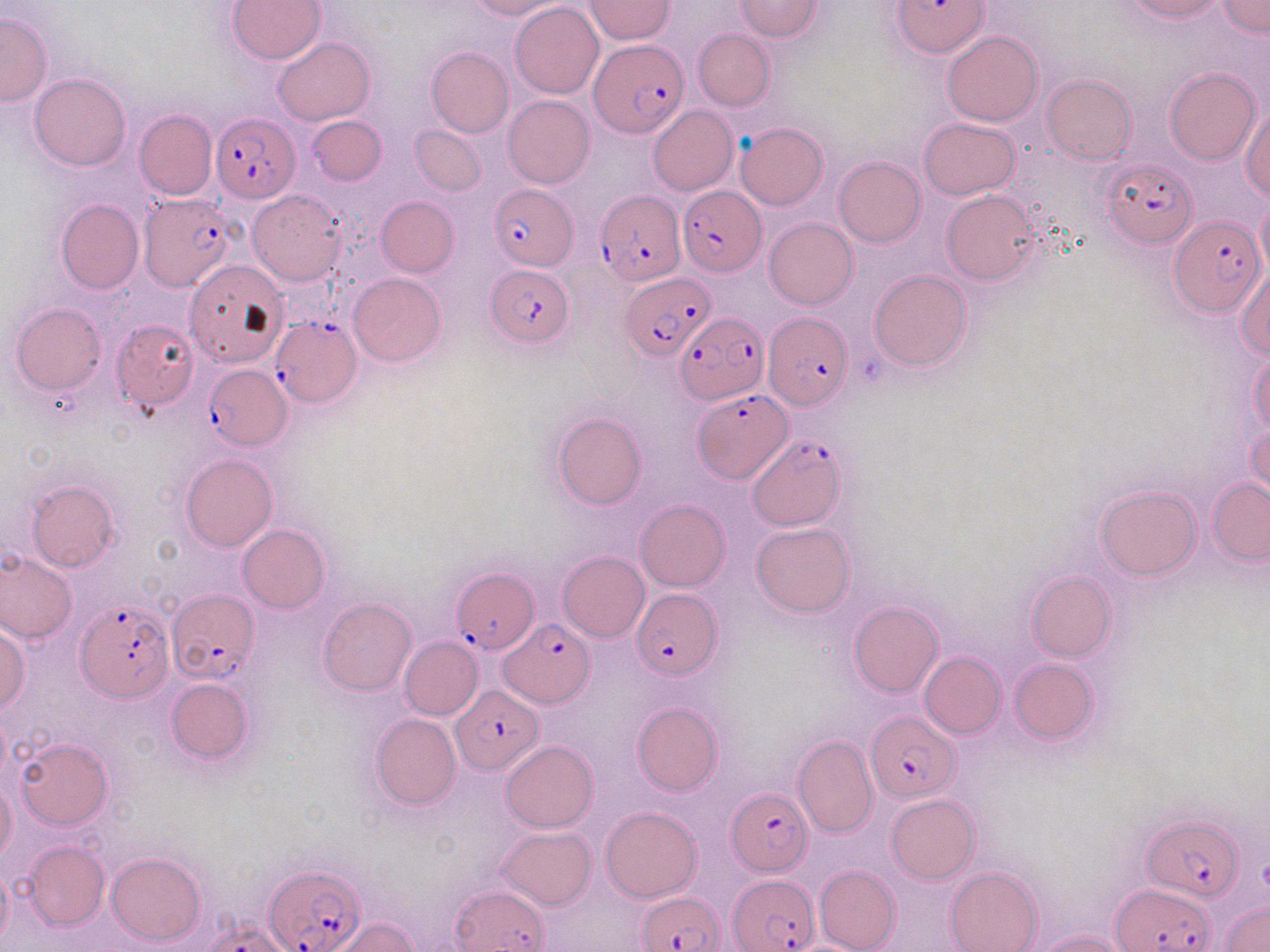
Approximate bounding boxes as (x1, y1, x2, y2) in pixels. Plasmodium falciparum-infected red blood cell locations: (891, 2, 988, 57), (591, 42, 688, 138), (212, 113, 301, 203), (1099, 156, 1198, 249), (489, 185, 579, 271), (677, 186, 763, 276), (597, 190, 685, 286), (140, 195, 234, 290), (1169, 215, 1264, 314), (486, 263, 571, 347), (622, 272, 715, 362), (676, 312, 768, 405), (763, 312, 851, 410), (267, 317, 359, 409), (204, 364, 291, 450), (693, 388, 791, 483), (746, 434, 844, 530), (452, 569, 538, 654), (166, 589, 257, 683), (633, 589, 721, 678), (76, 600, 174, 702), (502, 620, 593, 707), (451, 683, 544, 774), (866, 709, 958, 802), (724, 787, 814, 876), (1145, 814, 1244, 903), (264, 865, 363, 952), (728, 874, 819, 951), (1112, 882, 1214, 952), (639, 893, 724, 952). Uninfected red blood cell locations: (469, 0, 565, 19), (733, 0, 823, 41), (1120, 0, 1226, 22), (1219, 0, 1268, 37), (229, 1, 325, 64), (584, 1, 675, 43), (510, 2, 604, 99), (0, 11, 52, 107), (693, 29, 775, 111), (942, 30, 1042, 126), (273, 37, 374, 125), (426, 47, 513, 138), (1165, 68, 1258, 164), (29, 74, 132, 171), (1042, 74, 1137, 164), (502, 94, 594, 189), (647, 105, 738, 196), (1241, 105, 1270, 200), (135, 109, 218, 201), (307, 116, 386, 186), (919, 117, 1019, 200), (734, 122, 828, 209), (411, 126, 486, 196), (833, 156, 925, 247), (249, 190, 347, 286), (941, 191, 1043, 285), (375, 196, 459, 276), (1256, 196, 1270, 279), (55, 199, 143, 294), (764, 218, 857, 310), (184, 259, 288, 367), (1234, 264, 1270, 359), (868, 269, 971, 371), (348, 273, 445, 366), (12, 302, 106, 394), (111, 320, 198, 411), (1248, 350, 1269, 437), (553, 411, 646, 509), (1246, 418, 1270, 499), (181, 454, 277, 551), (25, 478, 119, 573), (1208, 478, 1270, 564), (1095, 486, 1200, 581), (635, 499, 730, 591), (751, 522, 855, 616), (237, 523, 329, 612), (0, 551, 77, 645), (557, 551, 649, 643), (1026, 571, 1116, 662), (318, 598, 416, 695), (848, 601, 941, 697), (0, 625, 28, 715), (399, 636, 482, 720), (920, 651, 1005, 738), (1009, 658, 1098, 744), (166, 678, 253, 763), (632, 702, 722, 796), (371, 713, 460, 809), (794, 734, 878, 838), (17, 737, 112, 829), (501, 740, 598, 832), (1, 780, 16, 864), (887, 794, 980, 883), (600, 806, 702, 901), (498, 827, 597, 909), (23, 840, 109, 930), (107, 852, 205, 946), (816, 865, 901, 952), (0, 866, 11, 947), (945, 866, 1041, 952), (453, 884, 549, 952), (1222, 902, 1270, 952), (330, 917, 421, 952), (203, 923, 295, 952), (1036, 929, 1132, 952). Slide-level diagnosis: Plasmodium falciparum. Optical microscopy. Image is 1270×952 pixels. Captured at 1000x magnification. Thin blood film. May-Grünwald-Giemsa-stained preparation. One field of a larger specimen.